Describe the morphology of the erythrocytes.
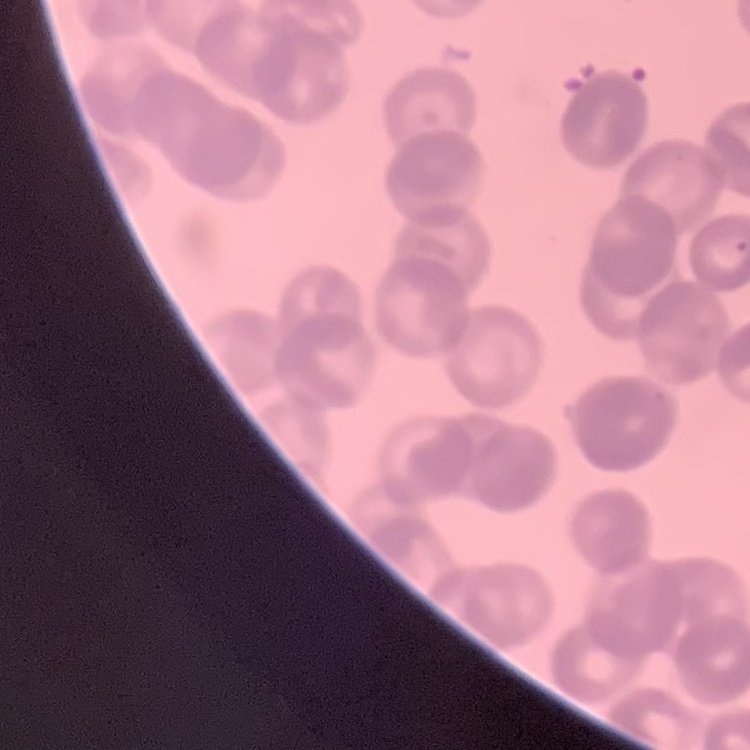

They show rouleaux formation.

{
  "stain": "Field's or Giemsa",
  "preparation": "thin peripheral smear",
  "image_type": "square crop of a larger photomicrograph"
}